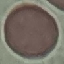

Result: negative for malaria parasites. Cell patch, automatically extracted from a larger field of view and resized to 64 × 64 pixels. Photographed with a smartphone camera at the microscope eyepiece. Giemsa stain. Thin smear of blood.